Outline each Plasmodium falciparum-infected red blood cell.
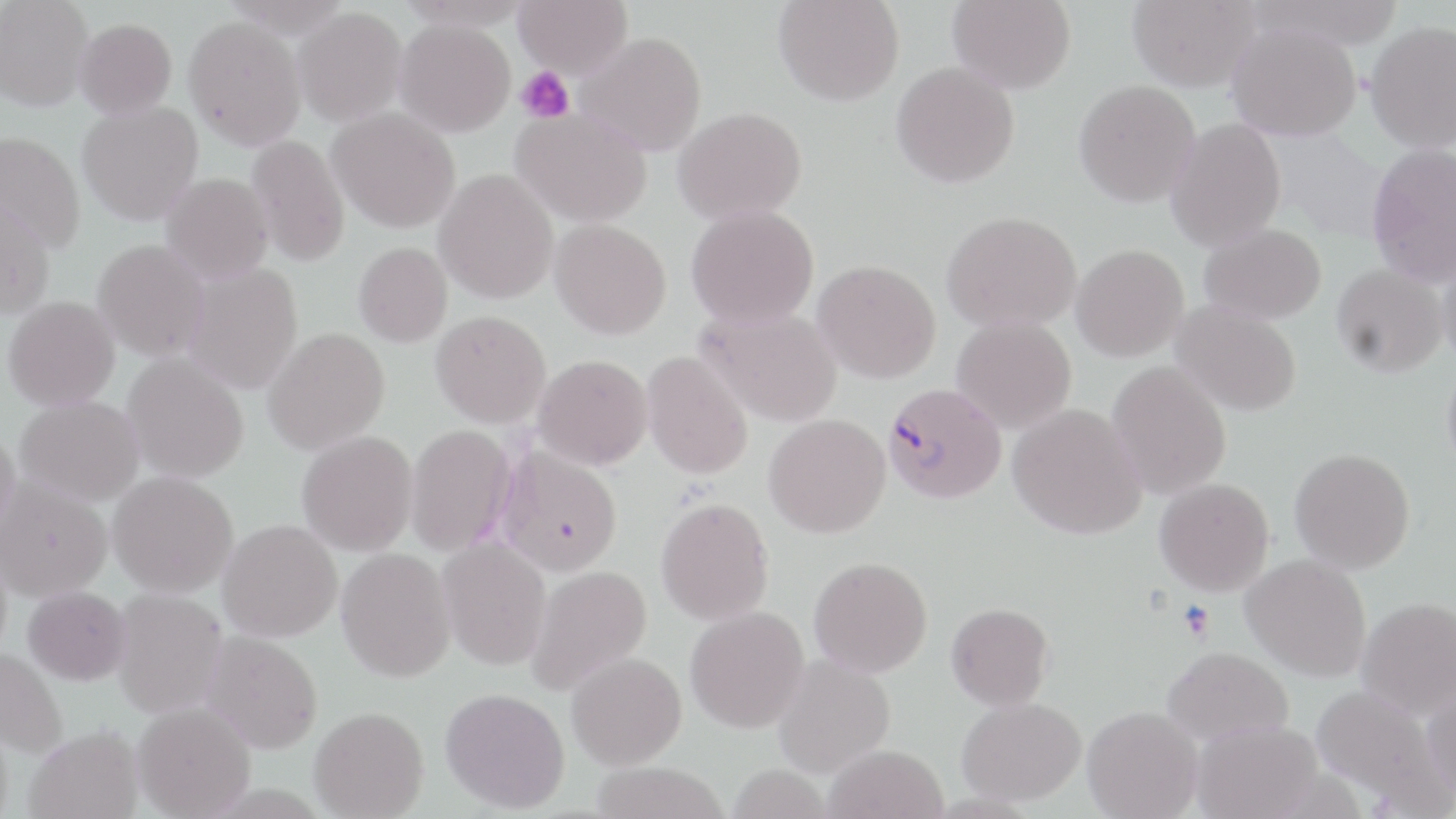
Approximate bounding boxes as named x1/y1/x2/y2 corners in pixels.
Plasmodium falciparum-infected red blood cells: (x1=884, y1=382, x2=1006, y2=504).

slide-level diagnosis = Plasmodium falciparum
field of view = single
stain = May-Grünwald-Giemsa
modality = optical microscopy
image size = 1456×819 pixels
magnification = 1000x
preparation = thin blood smear
platelet locations = approximate bounding boxes as named x1/y1/x2/y2 corners in pixels: (x1=515, y1=67, x2=575, y2=124), (x1=1178, y1=600, x2=1215, y2=641)
uninfected red blood cell locations = approximate bounding boxes as named x1/y1/x2/y2 corners in pixels: (x1=0, y1=0, x2=94, y2=112), (x1=397, y1=0, x2=535, y2=30), (x1=513, y1=0, x2=632, y2=79), (x1=773, y1=0, x2=905, y2=106), (x1=949, y1=0, x2=1076, y2=94), (x1=1128, y1=0, x2=1260, y2=92), (x1=1248, y1=0, x2=1405, y2=51), (x1=293, y1=6, x2=407, y2=127), (x1=183, y1=16, x2=306, y2=151), (x1=75, y1=18, x2=177, y2=119), (x1=395, y1=19, x2=516, y2=137), (x1=1365, y1=21, x2=1456, y2=153), (x1=1227, y1=22, x2=1362, y2=141), (x1=575, y1=31, x2=707, y2=157), (x1=891, y1=61, x2=1020, y2=188), (x1=1074, y1=79, x2=1200, y2=208), (x1=77, y1=101, x2=203, y2=225), (x1=673, y1=106, x2=807, y2=225), (x1=328, y1=107, x2=462, y2=233), (x1=511, y1=107, x2=652, y2=227), (x1=1165, y1=117, x2=1287, y2=251), (x1=0, y1=131, x2=86, y2=253), (x1=246, y1=134, x2=351, y2=268), (x1=1366, y1=142, x2=1456, y2=288), (x1=434, y1=168, x2=559, y2=304), (x1=161, y1=173, x2=274, y2=285), (x1=0, y1=196, x2=55, y2=320), (x1=685, y1=204, x2=820, y2=329), (x1=941, y1=210, x2=1081, y2=332), (x1=549, y1=218, x2=672, y2=340), (x1=1199, y1=223, x2=1327, y2=325), (x1=92, y1=239, x2=210, y2=362), (x1=353, y1=242, x2=452, y2=347), (x1=1071, y1=244, x2=1189, y2=362), (x1=1438, y1=249, x2=1456, y2=368), (x1=813, y1=260, x2=941, y2=384), (x1=182, y1=262, x2=304, y2=395), (x1=1331, y1=264, x2=1447, y2=377), (x1=3, y1=296, x2=120, y2=411), (x1=1170, y1=300, x2=1302, y2=416), (x1=697, y1=305, x2=843, y2=427), (x1=431, y1=310, x2=551, y2=428), (x1=952, y1=316, x2=1077, y2=433), (x1=262, y1=327, x2=390, y2=456), (x1=641, y1=350, x2=754, y2=481), (x1=122, y1=352, x2=249, y2=483), (x1=533, y1=354, x2=653, y2=470), (x1=1441, y1=358, x2=1456, y2=478), (x1=1107, y1=361, x2=1232, y2=500), (x1=14, y1=396, x2=144, y2=506), (x1=1008, y1=404, x2=1147, y2=540), (x1=764, y1=413, x2=891, y2=538), (x1=405, y1=423, x2=518, y2=556), (x1=0, y1=424, x2=20, y2=542), (x1=296, y1=430, x2=418, y2=556), (x1=494, y1=443, x2=623, y2=577), (x1=1290, y1=448, x2=1415, y2=574), (x1=107, y1=471, x2=239, y2=597), (x1=1, y1=477, x2=112, y2=601), (x1=1154, y1=478, x2=1274, y2=596), (x1=656, y1=497, x2=774, y2=626), (x1=218, y1=518, x2=343, y2=642), (x1=437, y1=537, x2=552, y2=671), (x1=336, y1=548, x2=456, y2=682), (x1=1242, y1=553, x2=1372, y2=682), (x1=809, y1=556, x2=933, y2=678), (x1=525, y1=565, x2=652, y2=696), (x1=23, y1=586, x2=131, y2=686), (x1=110, y1=588, x2=227, y2=718), (x1=1357, y1=597, x2=1456, y2=719), (x1=946, y1=602, x2=1054, y2=710), (x1=685, y1=605, x2=809, y2=733), (x1=200, y1=631, x2=324, y2=754), (x1=1162, y1=646, x2=1294, y2=746), (x1=0, y1=647, x2=68, y2=758), (x1=566, y1=651, x2=687, y2=770), (x1=772, y1=654, x2=897, y2=778), (x1=1422, y1=682, x2=1456, y2=805), (x1=1309, y1=684, x2=1449, y2=804), (x1=440, y1=687, x2=570, y2=813), (x1=956, y1=697, x2=1087, y2=806), (x1=132, y1=702, x2=256, y2=818), (x1=1082, y1=705, x2=1203, y2=819), (x1=309, y1=706, x2=429, y2=818), (x1=1191, y1=719, x2=1323, y2=819), (x1=25, y1=726, x2=144, y2=819), (x1=823, y1=743, x2=949, y2=819), (x1=589, y1=761, x2=730, y2=819), (x1=727, y1=763, x2=833, y2=819)